Identify the parasite.
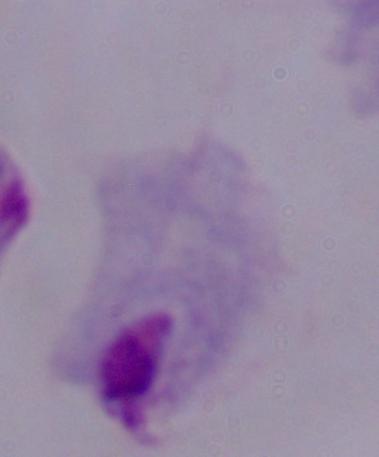

A trichomonad.

modality: micrograph
magnification: 1000x